State which parasite is depicted.
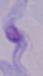

This is a trypanosome.

1000x magnification. Photomicrograph.